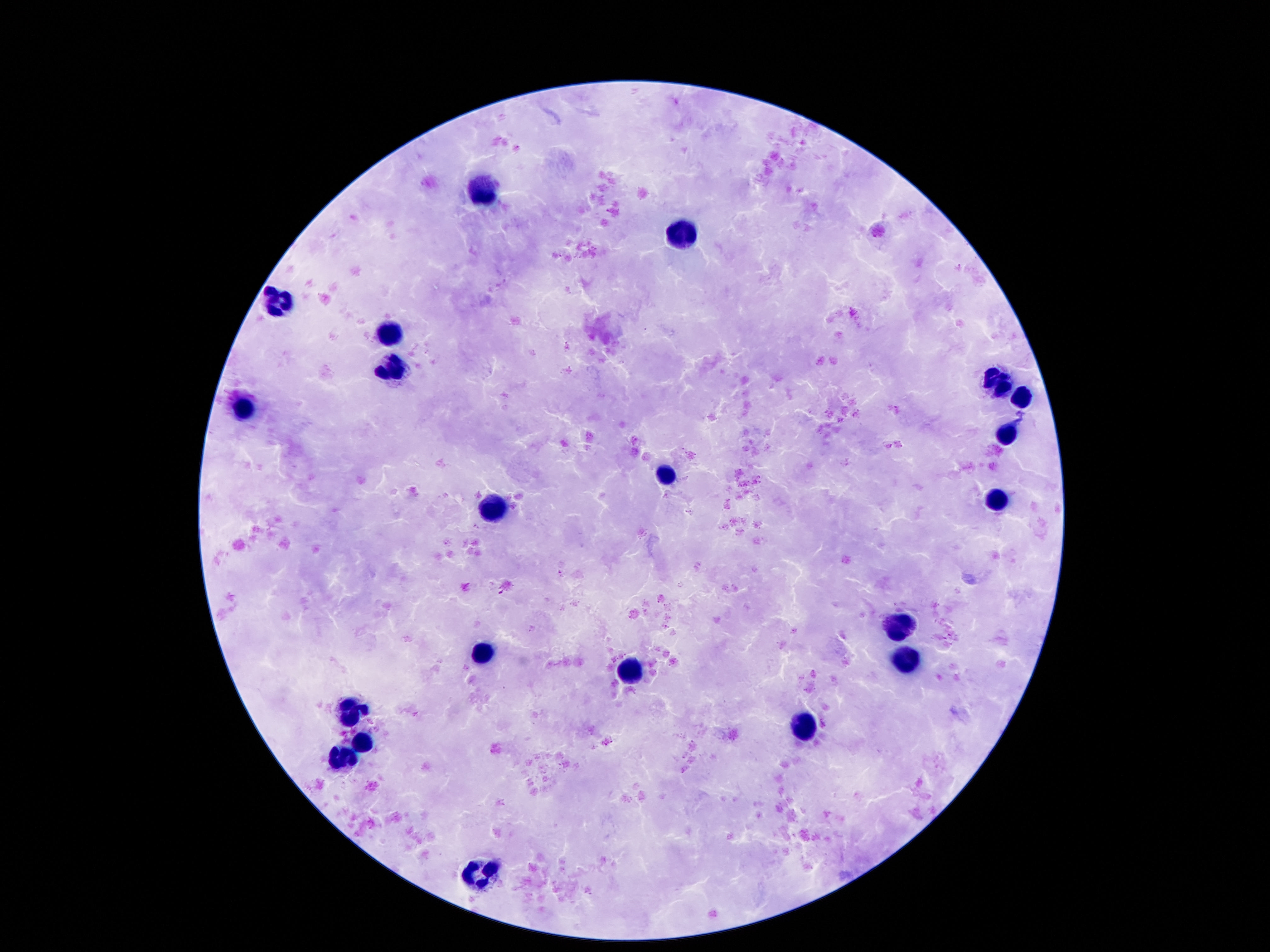 Approximate centers as [x, y] in pixels. Leukocyte locations: [485, 189], [680, 235], [277, 302], [394, 326], [390, 368], [997, 382], [1020, 397], [247, 407], [1005, 431], [667, 476], [997, 500], [493, 508], [898, 628], [482, 652], [905, 661], [629, 670], [350, 710], [800, 727], [361, 742], [344, 755], [482, 872]. Thick blood film. Photographed through the microscope eyepiece with a smartphone camera. Image is 1270×952 pixels. Single field of view. Patient malaria status: uninfected. Giemsa stain. 100x magnification.